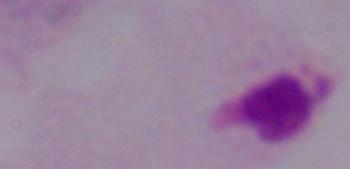 Photomicrograph. A trichomonad is shown. 1000x magnification.